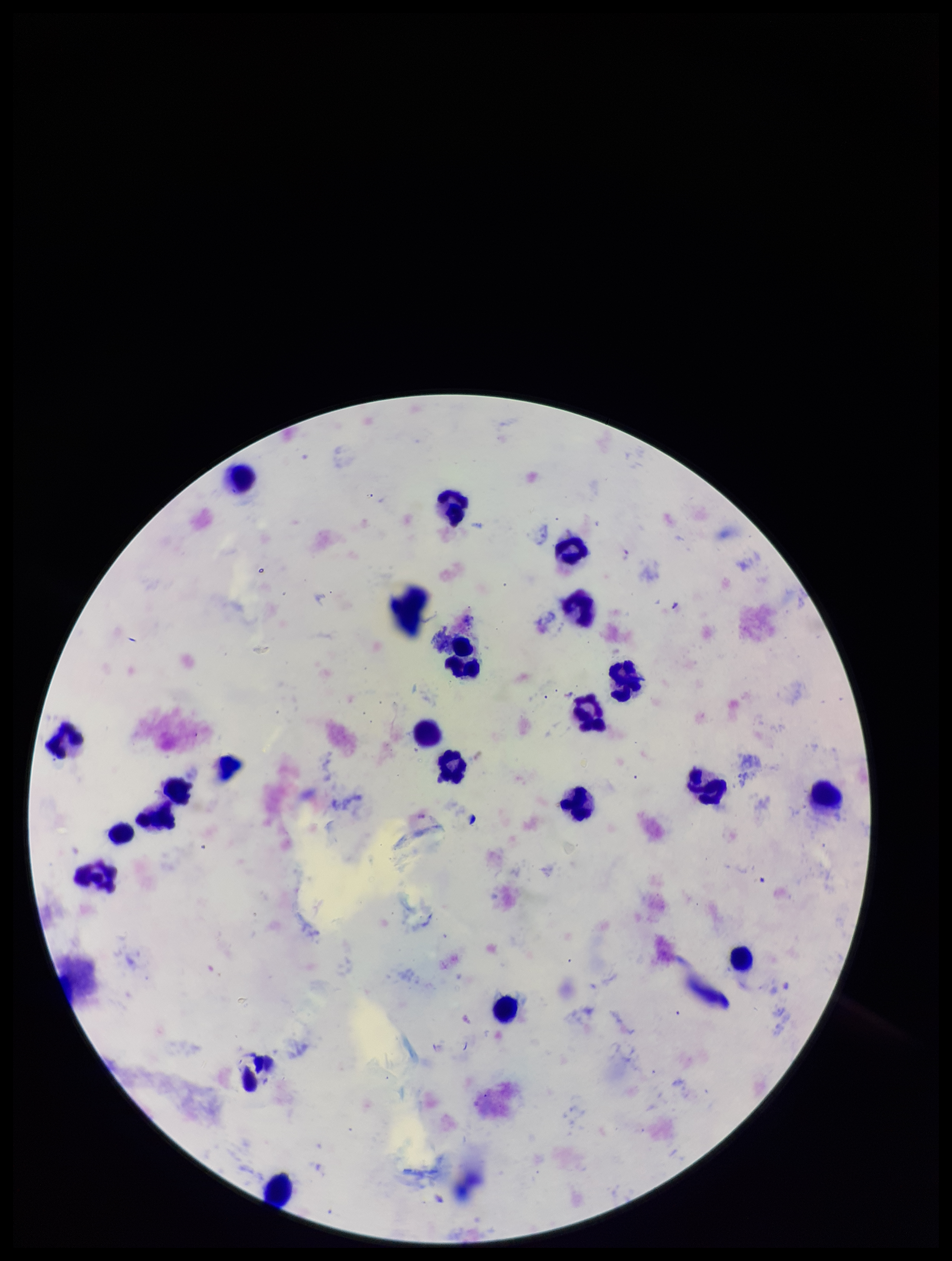

Preparation: thick blood smear. Plasmodium parasites: identified. Parasite count: 1. Giemsa stain. Species reported for this patient: Plasmodium falciparum. Photographed through the microscope eyepiece with a smartphone camera. Image is 952×1261 pixels. Patient malaria status: infected. Leukocyte count: 23. One field from this slide.